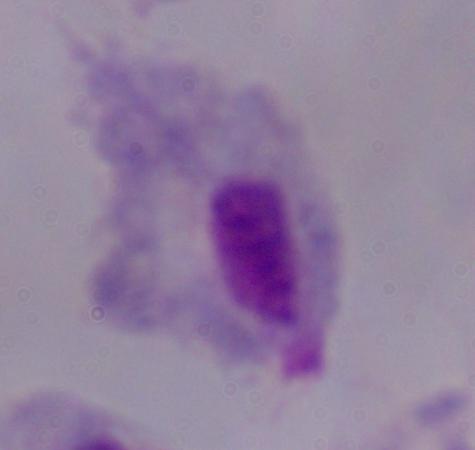

Summary:
  - Identification: trichomonad
  - Magnification: 1000x
  - Modality: photomicrograph